Assess this cell for malaria.
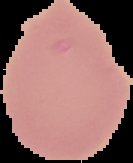
It is uninfected.

image_size: 133×163 pixels
image_type: segmented cell region with the area outside set to black
preparation: thin blood smear